Locate every Plasmodium parasite.
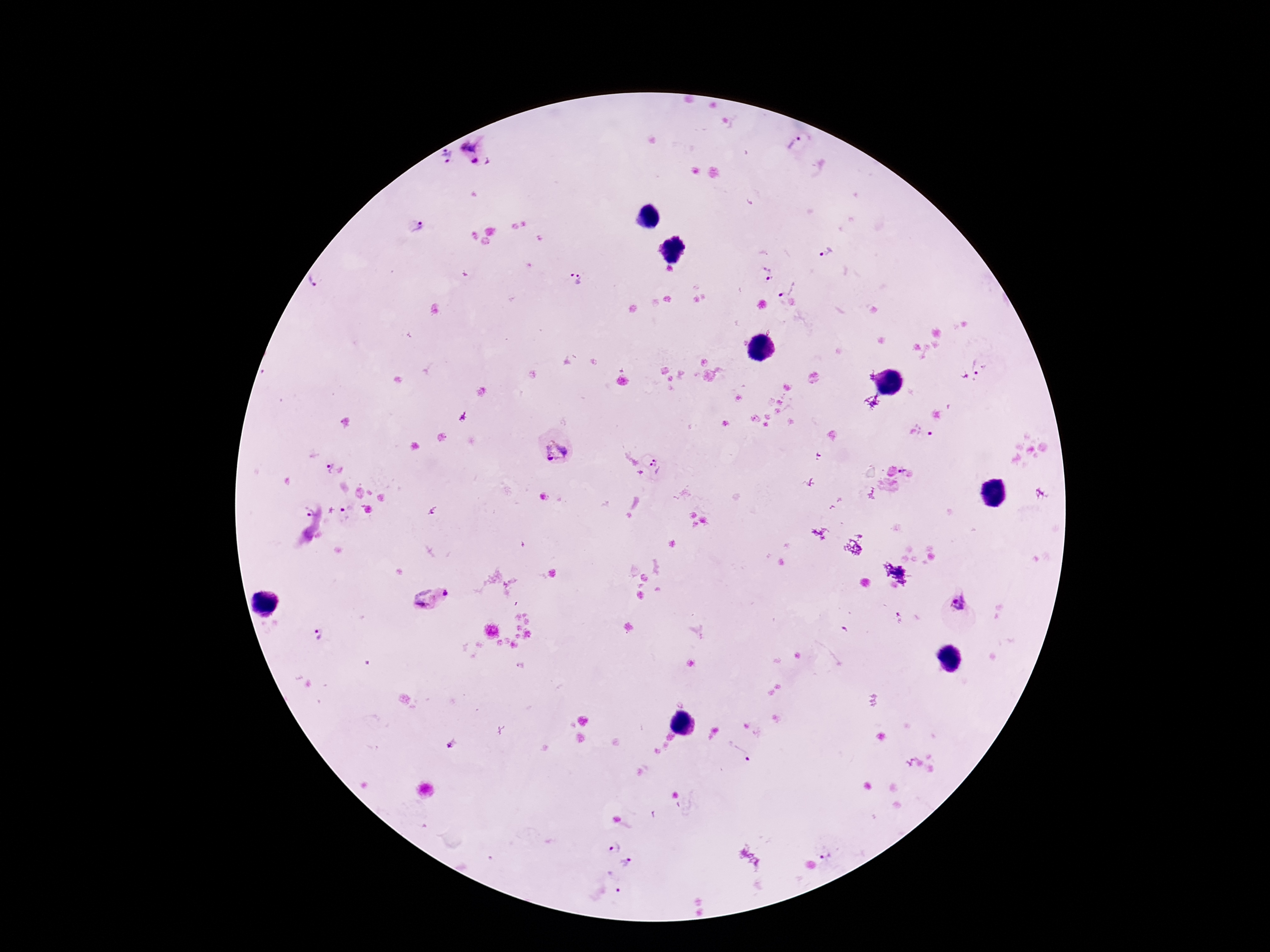
Approximate object centers, in pixels from the top-left corner.
Plasmodium parasites: (x=799, y=144), (x=471, y=145), (x=447, y=154), (x=475, y=160), (x=488, y=160), (x=418, y=226), (x=826, y=251), (x=767, y=273), (x=574, y=279), (x=318, y=283), (x=786, y=287), (x=979, y=366), (x=930, y=433), (x=549, y=455), (x=659, y=465), (x=327, y=467), (x=902, y=469), (x=306, y=509), (x=347, y=512), (x=444, y=592), (x=423, y=598), (x=958, y=601), (x=323, y=634), (x=452, y=743), (x=739, y=753), (x=614, y=846), (x=824, y=850), (x=626, y=861), (x=615, y=881).

image size = 1270×952 pixels
capture = smartphone camera through the microscope eyepiece
preparation = thick blood film
field of view = single
magnification = 100x
patient malaria status = positive
stain = Giemsa